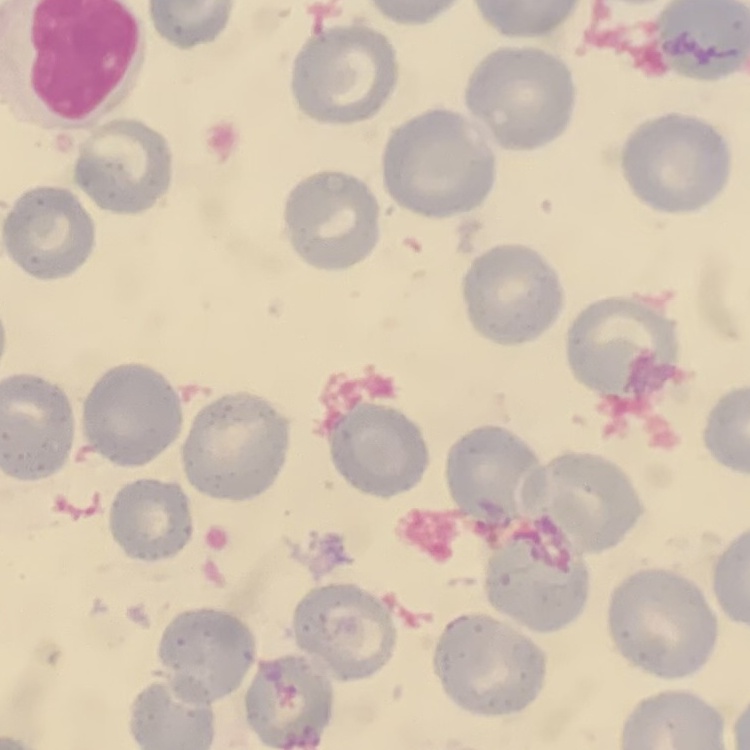 The erythrocytes exhibit no rouleaux formation. Square crop of a larger photomicrograph. Stained with either Field's or Giemsa. Thin blood smear.